Assess the morphology of the red blood cells.
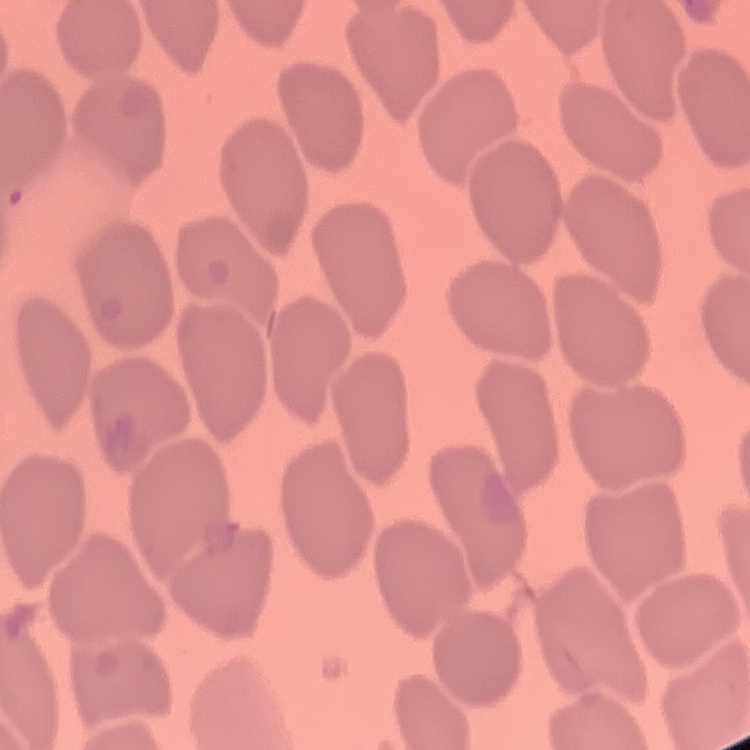
They show no rouleaux formation.

Summary:
  - Stain: Field's or Giemsa
  - Image type: one tile cut from a larger photomicrograph
  - Preparation: thin peripheral smear